Classify this cell by malaria status.
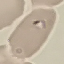

Parasitized.

image type = cell patch, automatically extracted from a larger field of view and resized to 64 × 64 pixels
preparation = thin smear
stain = Giemsa
capture = smartphone through the microscope eyepiece